Report the malaria status of this cell.
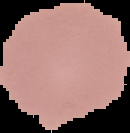

Uninfected.

From a thin blood film. Image is 130×133 pixels. Segmented cell region on a black background.